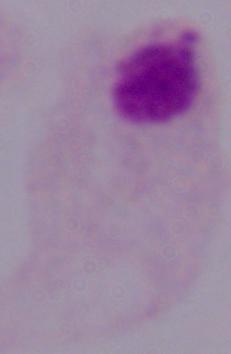
A trichomonad is seen. Photomicrograph. Captured at 1000x magnification.